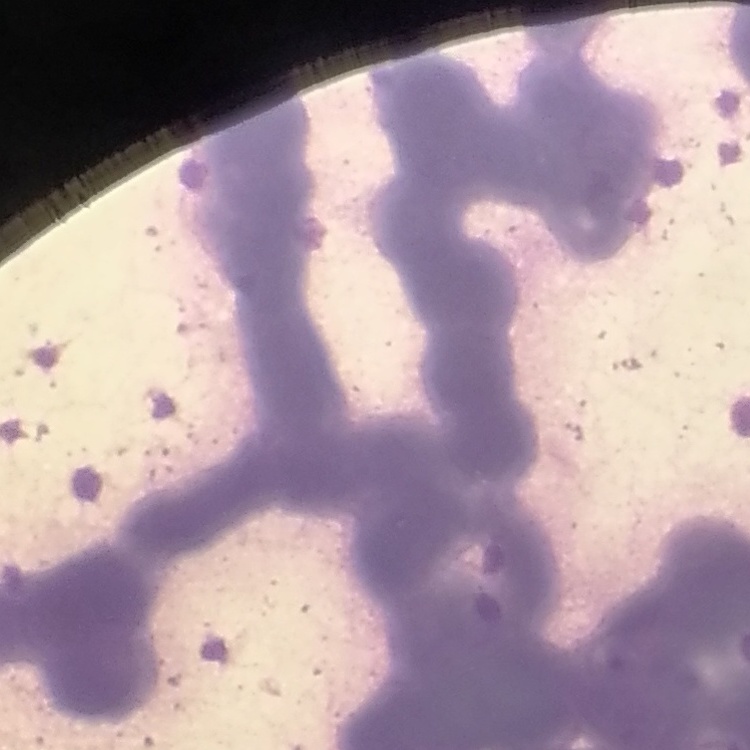
erythrocyte morphology = rouleaux formation
preparation = thin blood smear
image type = one tile cut from a larger photomicrograph
stain = Field's or Giemsa